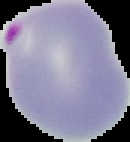
The area outside the segmented cell region is set to black. Image is 130×142 pixels. From a thin blood smear. Result: Plasmodium parasites identified.